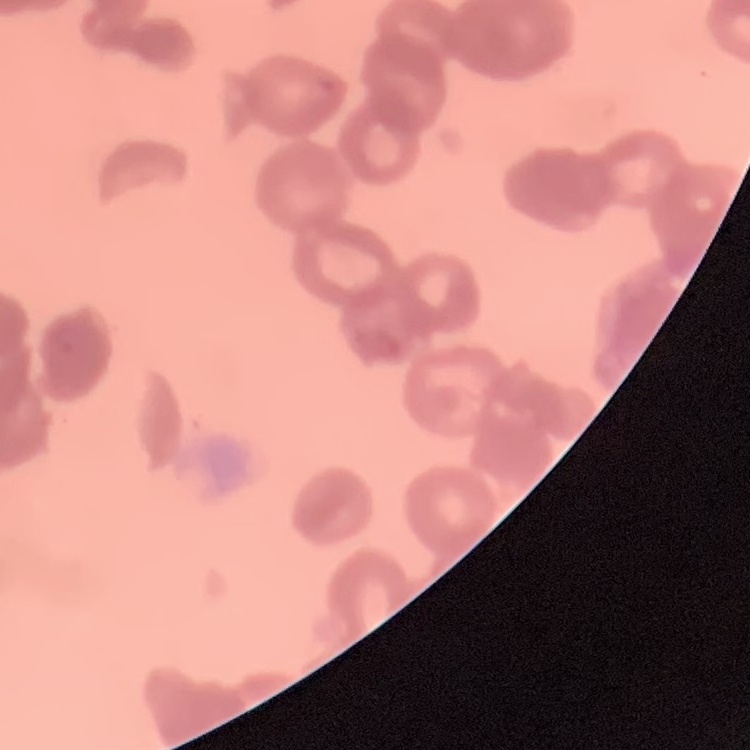
Summary:
  - Red blood cell morphology: rouleaux formation
  - Preparation: thin blood smear
  - Image type: square crop of a larger photomicrograph
  - Stain: Field's or Giemsa